Give the position of every Plasmodium parasite.
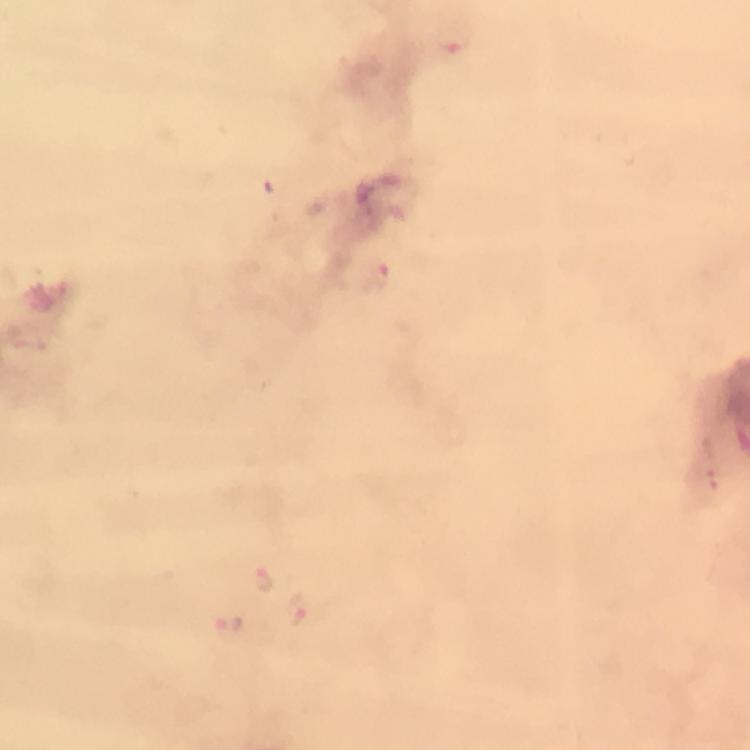
Approximate object centers, in pixels from the top-left corner.
Plasmodium parasites: (x=455, y=40), (x=377, y=278), (x=711, y=483), (x=268, y=579), (x=297, y=609), (x=231, y=624).

Summary:
  - Preparation: thick blood film
  - Image size: 750×750 pixels
  - Immersion oil: used
  - Capture: smartphone camera through the microscope
  - Magnification: 100x
  - Cropped from: a single field of view
  - Stain: Giemsa
  - Context: from a malaria diagnostic workup